Outline platelets.
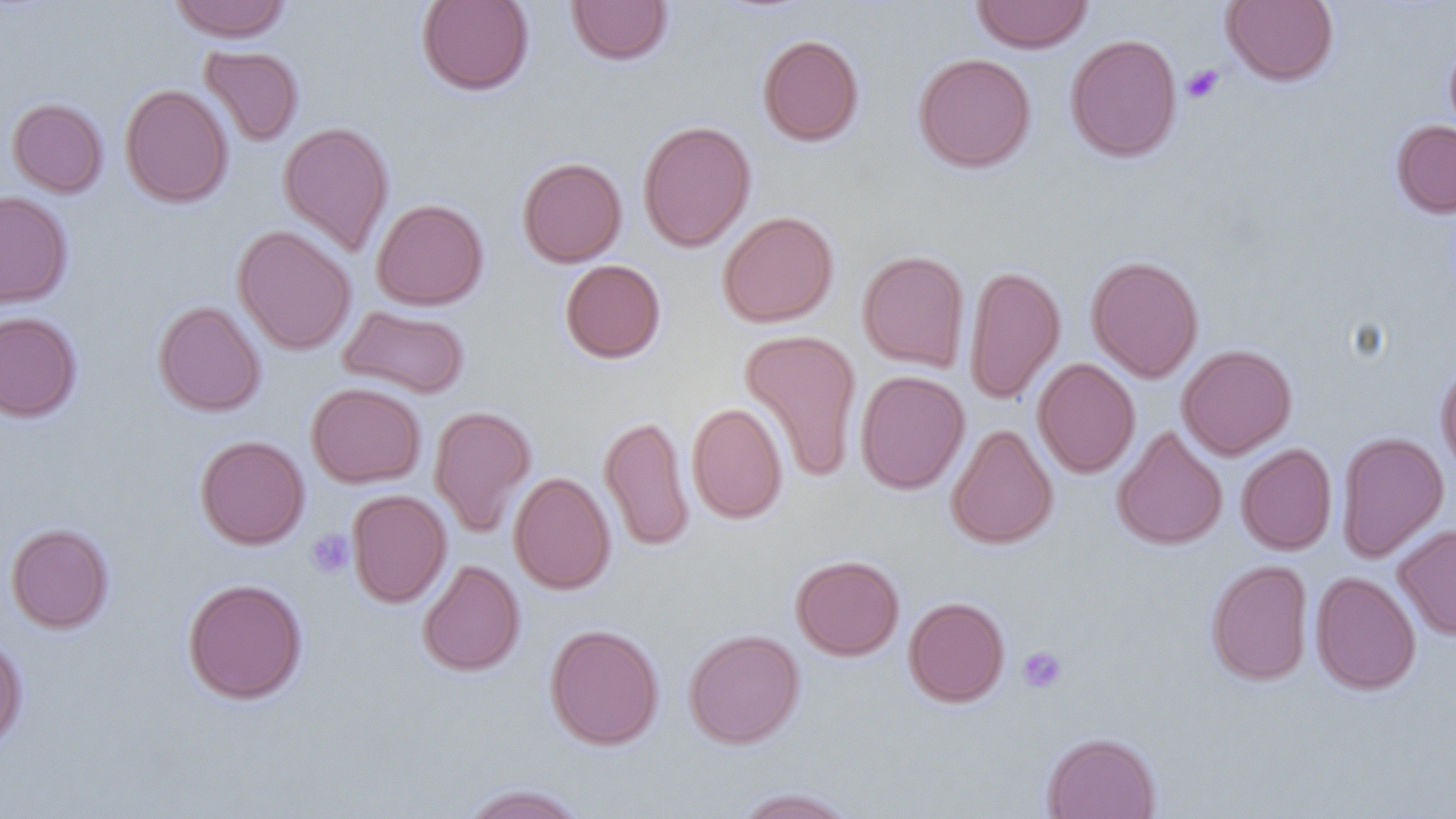

Approximate bounding boxes as (x1,y1)-(x2,y2) corner pairs in pixels.
Platelets: (1182,64)-(1223,103), (306,529)-(354,578), (1017,645)-(1068,694).

Uninfected red blood cell locations: (168,0)-(292,42), (417,0)-(534,96), (566,0)-(673,66), (970,0)-(1093,53), (1222,0)-(1339,86), (1065,33)-(1183,163), (757,34)-(865,147), (1444,37)-(1456,144), (199,45)-(304,147), (913,53)-(1035,173), (120,83)-(233,209), (6,97)-(109,198), (1391,119)-(1456,218), (278,120)-(394,257), (637,120)-(757,252), (517,157)-(627,268), (0,190)-(73,309), (371,198)-(488,311), (718,210)-(839,328), (232,225)-(356,355), (858,250)-(970,373), (1086,255)-(1204,382), (560,259)-(666,363), (964,263)-(1066,405), (153,300)-(266,417), (338,305)-(470,399), (0,311)-(83,423), (739,328)-(862,483), (1177,344)-(1297,460), (1032,358)-(1140,478), (1435,361)-(1456,480), (855,370)-(970,494), (306,382)-(427,488), (686,402)-(788,524), (429,405)-(537,538), (599,415)-(695,553), (946,423)-(1058,549), (1112,425)-(1228,551), (1336,430)-(1449,563), (195,435)-(310,550), (1236,443)-(1337,555), (508,471)-(616,595), (347,490)-(451,608), (5,522)-(114,633), (1393,524)-(1456,640), (790,554)-(904,661), (417,559)-(525,676), (1206,559)-(1314,686), (1311,571)-(1421,695), (182,578)-(308,704), (903,596)-(1011,707), (545,623)-(664,750), (684,628)-(804,749), (0,634)-(28,750), (1040,731)-(1162,819), (460,783)-(588,819), (731,787)-(860,818). Slide-level diagnosis: negative for blood parasites. Image is 1456×819 pixels. Thin blood smear. Captured at 1000x magnification. Optical microscopy. Single field of view.